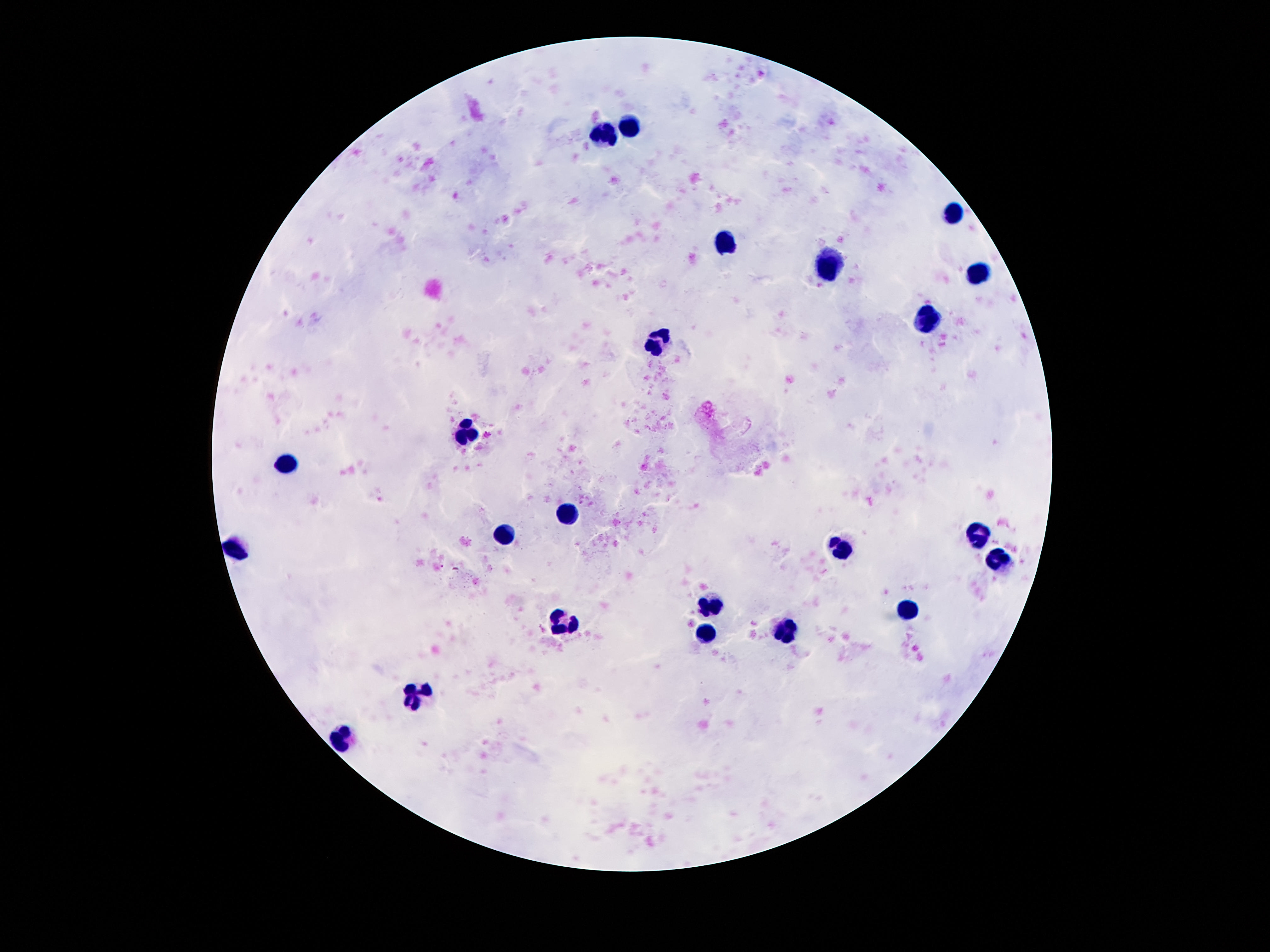
stain = Giemsa
patient malaria status = uninfected
magnification = 100x
preparation = thick blood film
field of view = one from this slide
leukocyte locations = approximate centers as [x, y] in pixels: [631, 127], [606, 134], [950, 208], [723, 246], [827, 264], [977, 272], [928, 320], [657, 338], [467, 434], [284, 465], [569, 514], [504, 535], [981, 535], [235, 545], [838, 548], [1000, 561], [713, 606], [907, 610], [563, 624], [788, 629], [706, 633], [422, 692], [346, 741]
capture = smartphone camera through the microscope eyepiece
image size = 1270×952 pixels